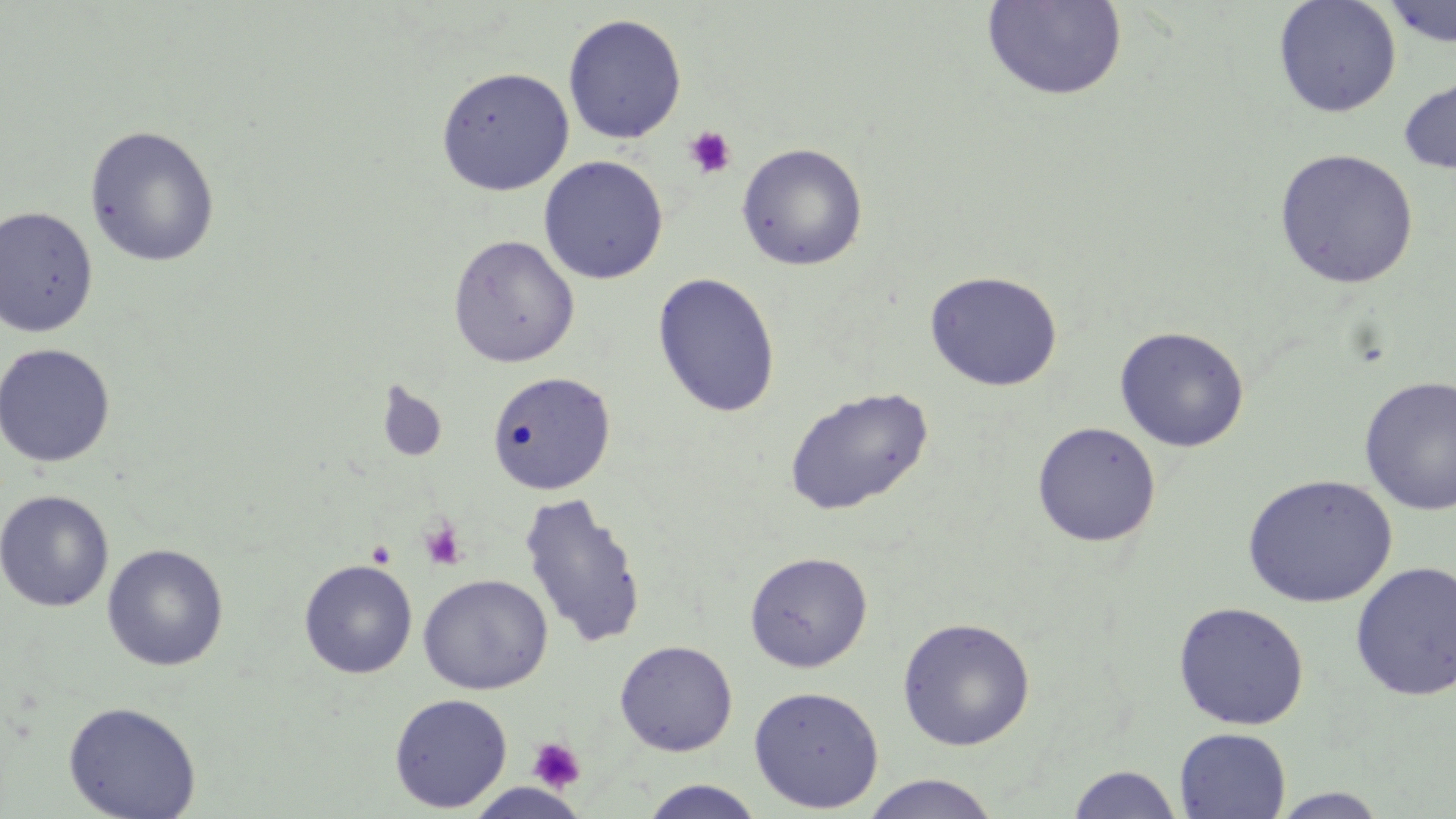

Summary:
  - Coordinate format: approximate bounding boxes as (x1,y1)-(x2,y2) corner pairs in pixels
  - Uninfected red blood cell locations: (1273,0)-(1401,118), (981,1)-(1128,102), (1381,1)-(1456,48), (562,13)-(687,144), (436,66)-(574,195), (1398,73)-(1456,175), (83,123)-(221,267), (736,142)-(869,271), (1274,148)-(1419,288), (538,155)-(669,285), (0,205)-(99,338), (447,233)-(579,367), (925,270)-(1063,391), (652,272)-(781,417), (1114,326)-(1250,452), (0,343)-(116,468), (486,370)-(616,496), (1359,376)-(1456,516), (376,381)-(447,463), (784,386)-(933,515), (1031,421)-(1161,547), (1241,474)-(1398,608), (1,489)-(114,613), (519,491)-(647,650), (101,543)-(229,671), (744,551)-(873,672), (299,559)-(417,679), (1350,560)-(1456,701), (418,573)-(553,695), (1172,601)-(1309,730), (897,617)-(1036,751), (614,640)-(737,756), (748,684)-(884,812), (389,693)-(513,812), (62,700)-(201,818), (1174,727)-(1291,818), (1067,764)-(1183,818), (860,774)-(1003,819), (639,780)-(764,818), (1269,787)-(1390,818)
  - Platelet locations: (682,125)-(738,180), (419,520)-(467,571), (366,540)-(396,567), (527,737)-(586,793)
  - Slide-level diagnosis: no evidence of blood parasites
  - Magnification: 1000x
  - Stain: May-Grünwald-Giemsa
  - Modality: light microscopy
  - Field of view: single
  - Image size: 1456×819 pixels
  - Preparation: thin blood smear